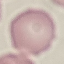
Result: no malaria parasites detected. Acquired by smartphone through the microscope eyepiece. Cell patch, automatically extracted from a larger field of view and resized to 64 × 64 pixels. Thin blood smear. Giemsa stain.